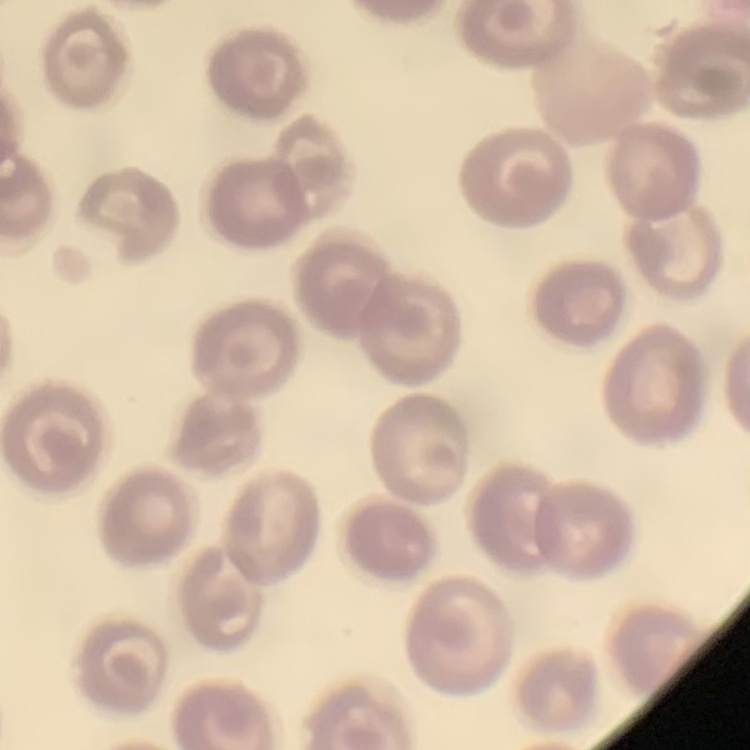

erythrocyte morphology = no rouleaux formation
stain = Field's or Giemsa
preparation = thin peripheral smear
image type = square crop of a larger photomicrograph